Identify the parasite.
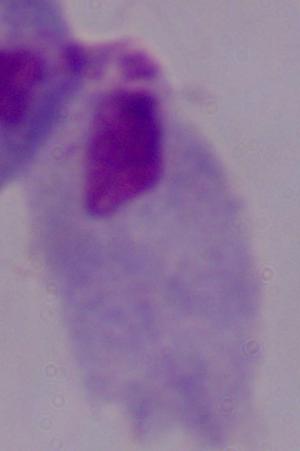

A trichomonad.

Captured at 1000x magnification. Micrograph.